Name the parasite shown.
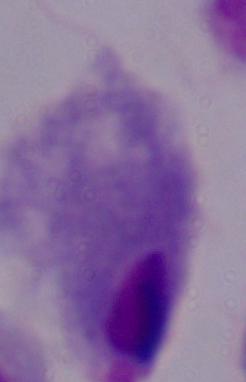
This is a trichomonad.

Captured at 1000x magnification. Photomicrograph.